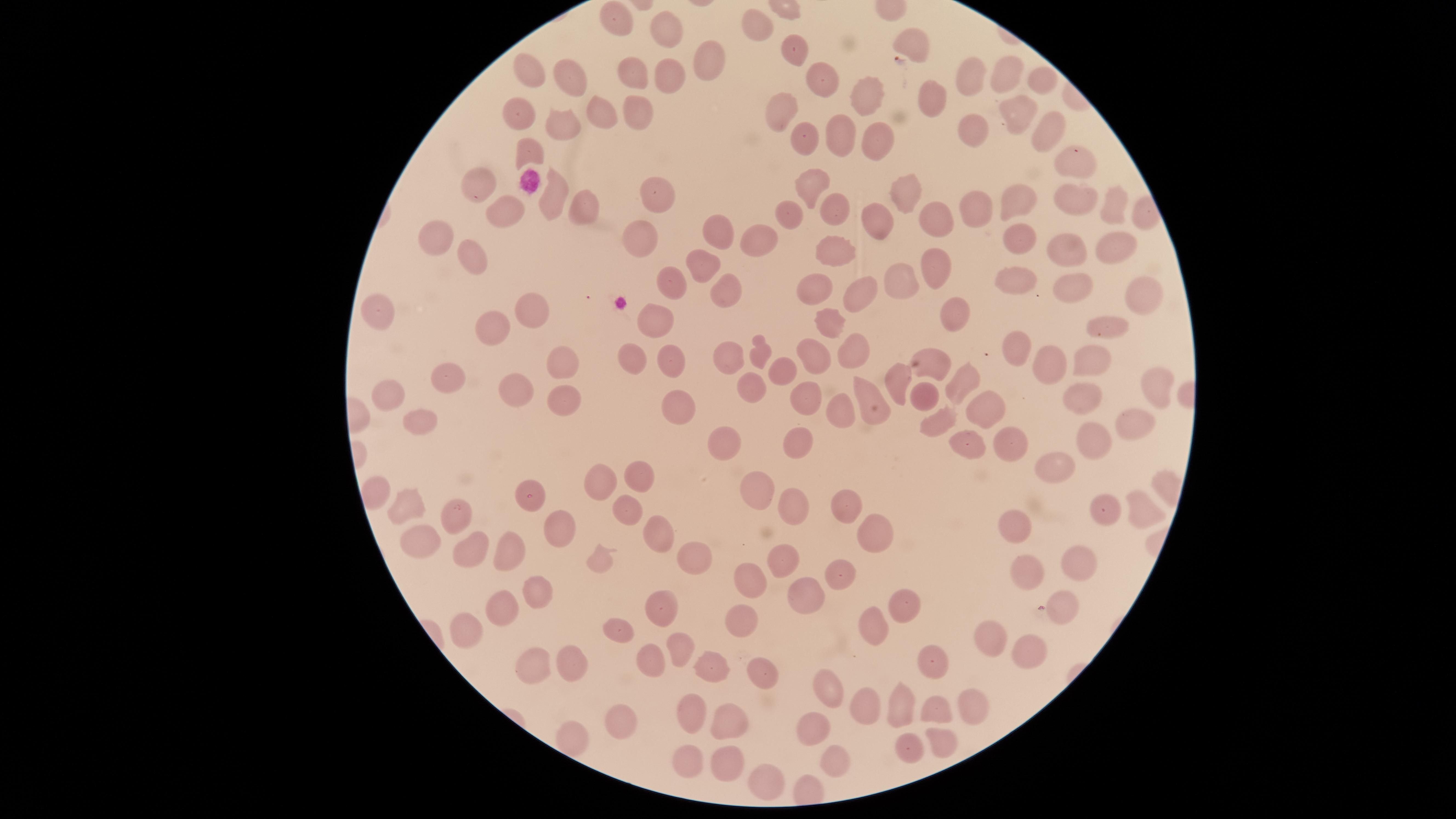

Approximate marker points as [x, y] in pixels.
Summary:
  - Uninfected red blood cells: [613, 11], [757, 23], [664, 27], [911, 41], [800, 56], [717, 60], [525, 76], [826, 77], [566, 78], [634, 78], [667, 78], [1009, 78], [1046, 81], [974, 82], [866, 95], [930, 101], [784, 104], [1001, 108], [635, 109], [513, 113], [598, 116], [1049, 127], [969, 128], [564, 130], [841, 133], [808, 141], [877, 142], [528, 152], [1073, 160], [807, 182], [476, 183], [907, 189], [655, 194], [547, 197], [1022, 202], [1078, 202], [505, 204], [838, 205], [577, 208], [975, 209], [1113, 209], [794, 213], [935, 217], [885, 219], [717, 226], [435, 236], [641, 237], [1016, 237], [756, 247], [460, 248], [1117, 248], [834, 250], [1064, 250], [937, 263], [706, 267], [1015, 280], [669, 281], [905, 281], [724, 289], [1077, 289], [817, 291], [1143, 292], [859, 294], [378, 308], [957, 311], [531, 313], [654, 319], [824, 322], [492, 326], [1106, 333], [1013, 345], [850, 349], [764, 352], [815, 352], [729, 356], [677, 357], [635, 358], [1083, 358], [1047, 361], [565, 363], [782, 368], [935, 369], [457, 377], [894, 380], [1150, 380], [966, 382], [869, 388], [748, 389], [510, 390], [1077, 394], [390, 396], [811, 396], [563, 399], [680, 407], [845, 411], [1139, 419], [411, 424], [1092, 442], [801, 444], [733, 445], [1058, 466], [642, 477], [604, 482], [757, 487], [530, 495], [412, 505], [843, 505], [1134, 505], [457, 507], [1101, 509], [628, 510], [793, 510], [1012, 527], [562, 529], [658, 535], [878, 537], [421, 542], [467, 551], [513, 551], [690, 560], [782, 560], [1081, 561], [1029, 564], [842, 578], [751, 585], [536, 590], [807, 595], [662, 602], [900, 602], [504, 607], [1069, 608], [747, 626], [869, 627], [621, 628], [473, 632], [991, 636], [679, 645], [1033, 650], [644, 657], [930, 658], [706, 663], [535, 665], [574, 667], [760, 669], [826, 689], [973, 702], [899, 703], [934, 704], [874, 706], [692, 707], [727, 719], [627, 720], [809, 727], [572, 736], [939, 737], [910, 748], [693, 760], [734, 760], [829, 763], [767, 775]
  - Capture: smartphone photograph through the microscope eyepiece
  - Image size: 1456×819 pixels
  - Field of view: single
  - Stain: Giemsa
  - Visible region: circular
  - Preparation: thin smear of blood
  - Presence: no malaria parasites identified